Locate and identify every blood parasite.
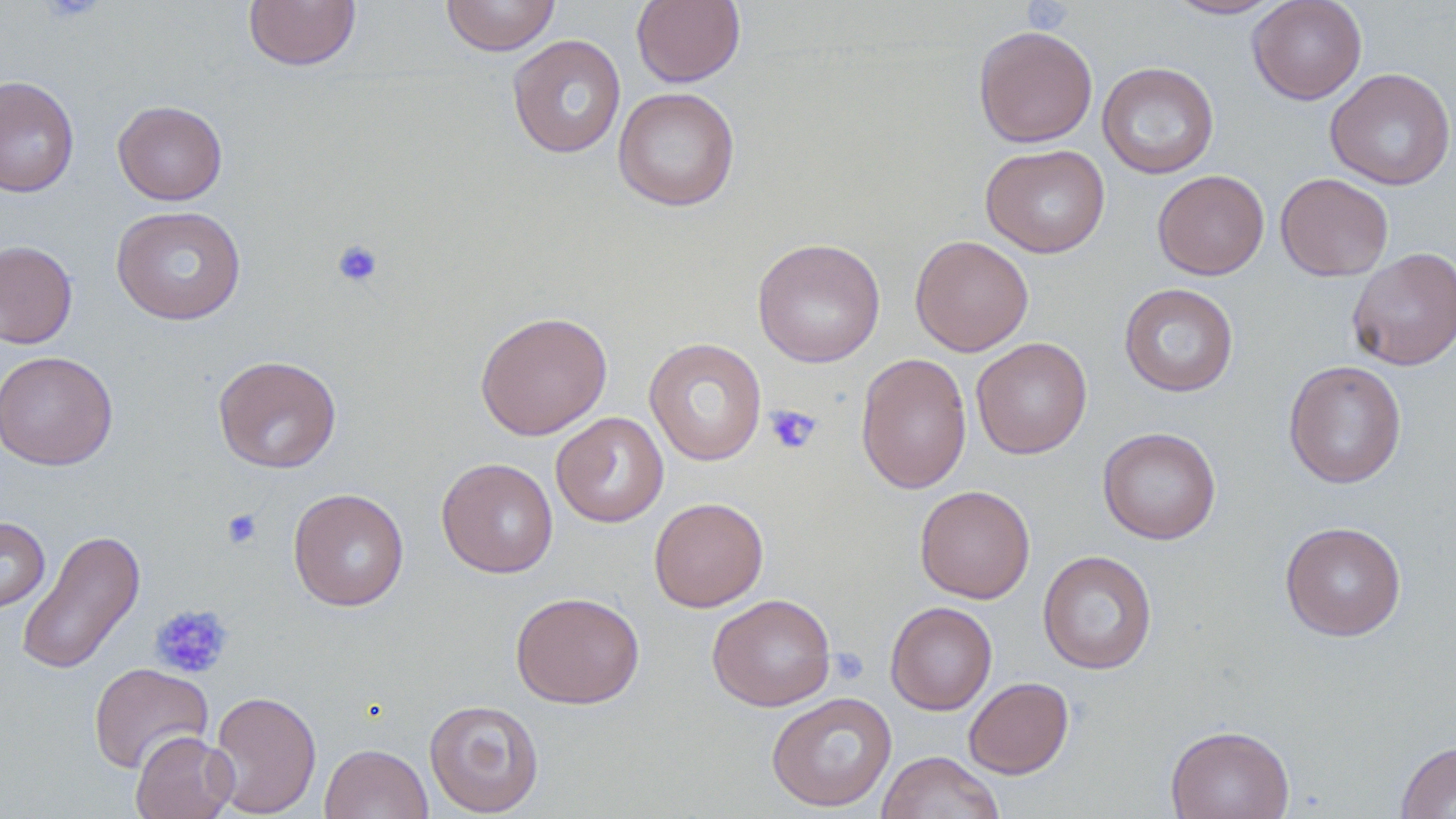

No blood parasites seen.

slide-level diagnosis = negative for blood parasites
platelet locations = approximate bounding boxes as (x1,y1)-(x2,y2) corner pairs in pixels: (330,239)-(384,289), (764,404)-(822,455), (221,508)-(263,550), (149,604)-(235,680), (829,648)-(868,685)
field of view = single
uninfected red blood cell locations = approximate bounding boxes as (x1,y1)-(x2,y2) corner pairs in pixels: (440,0)-(561,56), (631,0)-(746,87), (1165,0)-(1286,20), (1247,0)-(1367,105), (244,1)-(361,71), (973,25)-(1097,148), (507,34)-(626,159), (1097,61)-(1219,179), (1324,68)-(1456,190), (0,76)-(80,198), (613,87)-(740,212), (113,100)-(228,205), (980,143)-(1111,258), (1152,169)-(1269,280), (1276,172)-(1394,281), (111,205)-(247,325), (910,234)-(1034,356), (752,238)-(886,367), (0,239)-(78,349), (1346,247)-(1456,371), (1119,283)-(1239,397), (475,311)-(613,440), (971,337)-(1092,459), (644,338)-(767,466), (0,350)-(117,470), (855,352)-(972,495), (213,355)-(342,473), (1283,360)-(1407,488), (551,412)-(668,528), (1097,427)-(1221,544), (436,458)-(559,578), (914,485)-(1035,603), (288,488)-(410,611), (650,497)-(768,612), (0,516)-(50,614), (1280,521)-(1406,641), (17,528)-(146,676), (1038,549)-(1157,675), (510,591)-(645,709), (707,593)-(835,711), (885,601)-(997,715), (88,662)-(213,775), (963,677)-(1074,779), (207,690)-(322,818), (766,692)-(897,812), (424,699)-(544,817), (1165,724)-(1295,819), (131,730)-(237,819), (1395,740)-(1456,818), (320,743)-(433,819), (877,750)-(1006,819)
modality = optical microscopy
magnification = 1000x
image size = 1456×819 pixels
stain = May-Grünwald-Giemsa
preparation = thin blood film